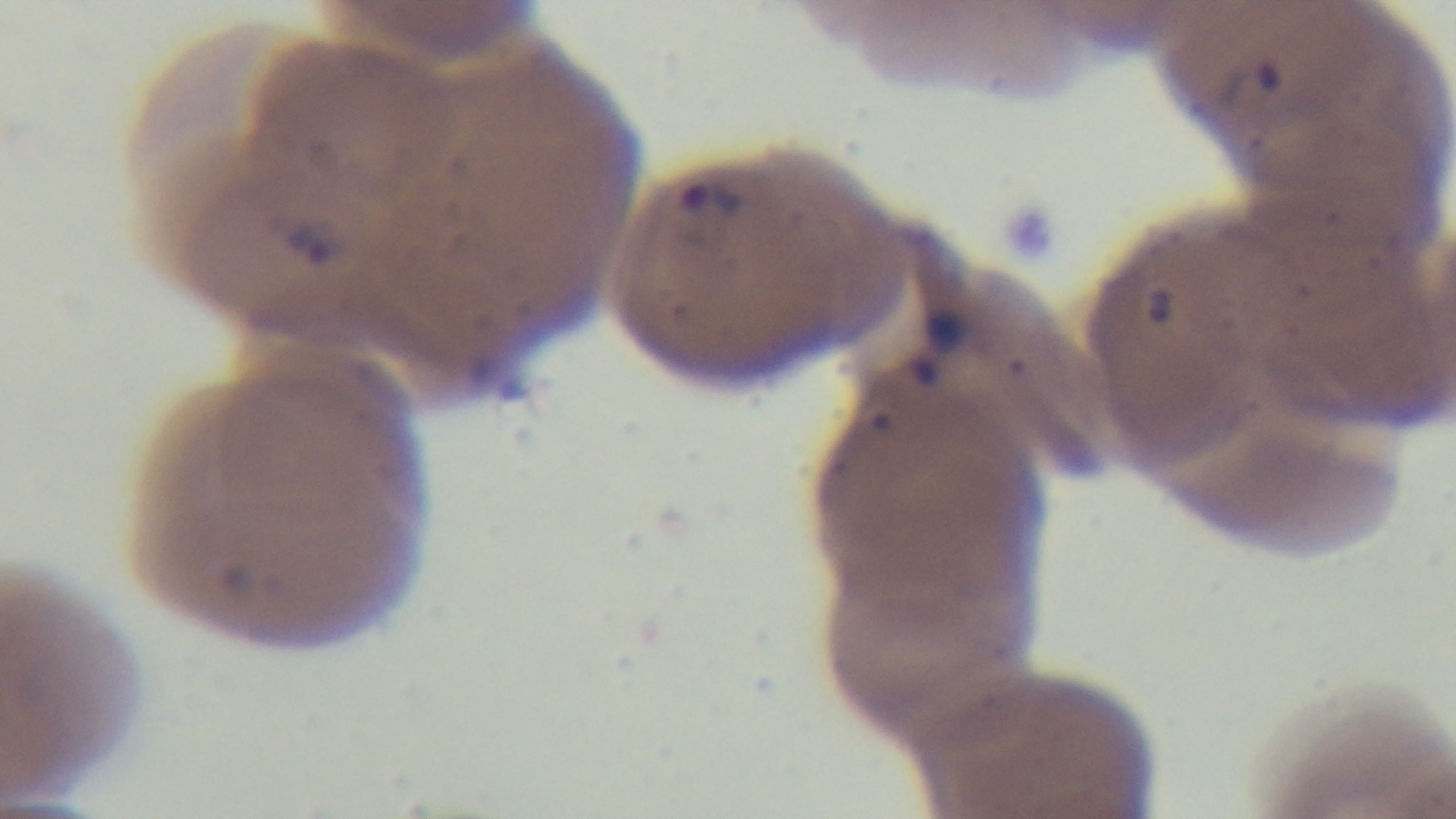

capture = mounted 4K digital camera
objective = 100x oil immersion
stain = Giemsa
preparation = thin blood film
field of view = single
malaria status = infected
modality = light microscopy